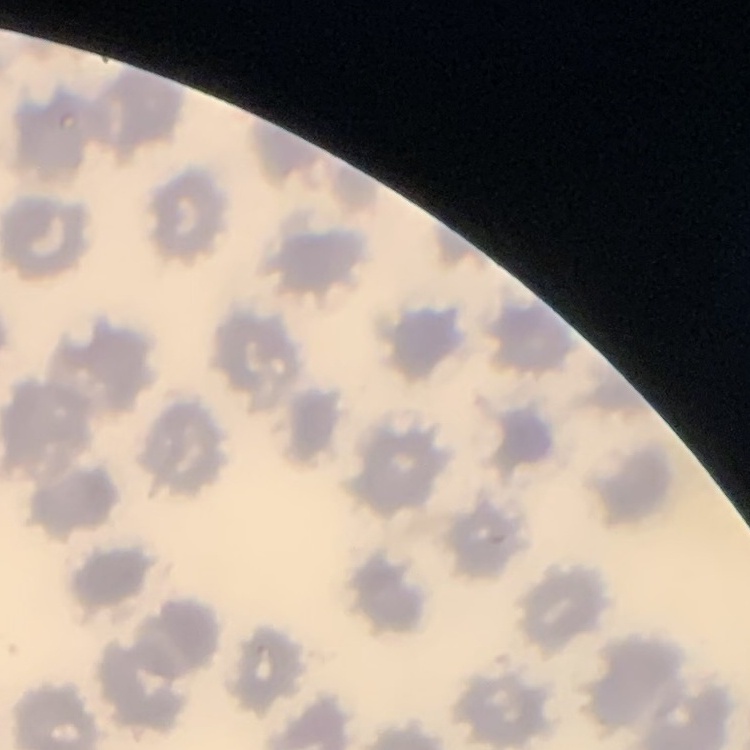
red_blood_cell_morphology: no rouleaux formation
image_type: one tile cut from a larger photomicrograph
preparation: thin peripheral smear
stain: Field's or Giemsa